Report the malaria status of this cell.
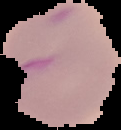

Parasitized.

Summary:
  - Image size: 121×130 pixels
  - Preparation: thin blood smear
  - Image type: segmented cell region with the area outside set to black